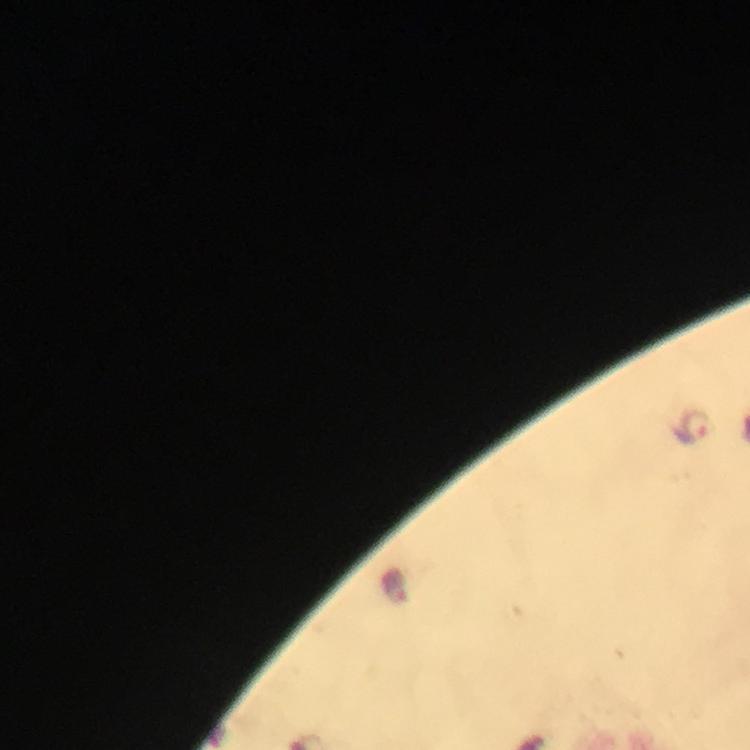

Approximate centers as {x, y} in pixels. Malaria parasite locations: {694, 427}. Thick smear. Image is 750×750 pixels. Giemsa-stained preparation. Cropped region of a single field of view. From a diagnostic examination for malaria. Immersion oil applied. 100x magnification. Smartphone photograph taken through a microscope.